Identify the parasite.
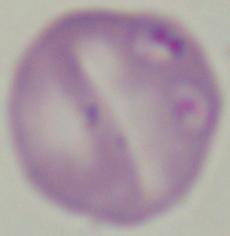
This is Babesia.

1000x magnification. Micrograph.